Classify this cell by malaria status.
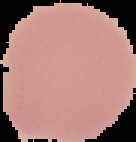
Uninfected.

Summary:
  - Image type: segmented cell region with the area outside set to black
  - Preparation: thin blood smear
  - Image size: 136×142 pixels